State the blood parasite species.
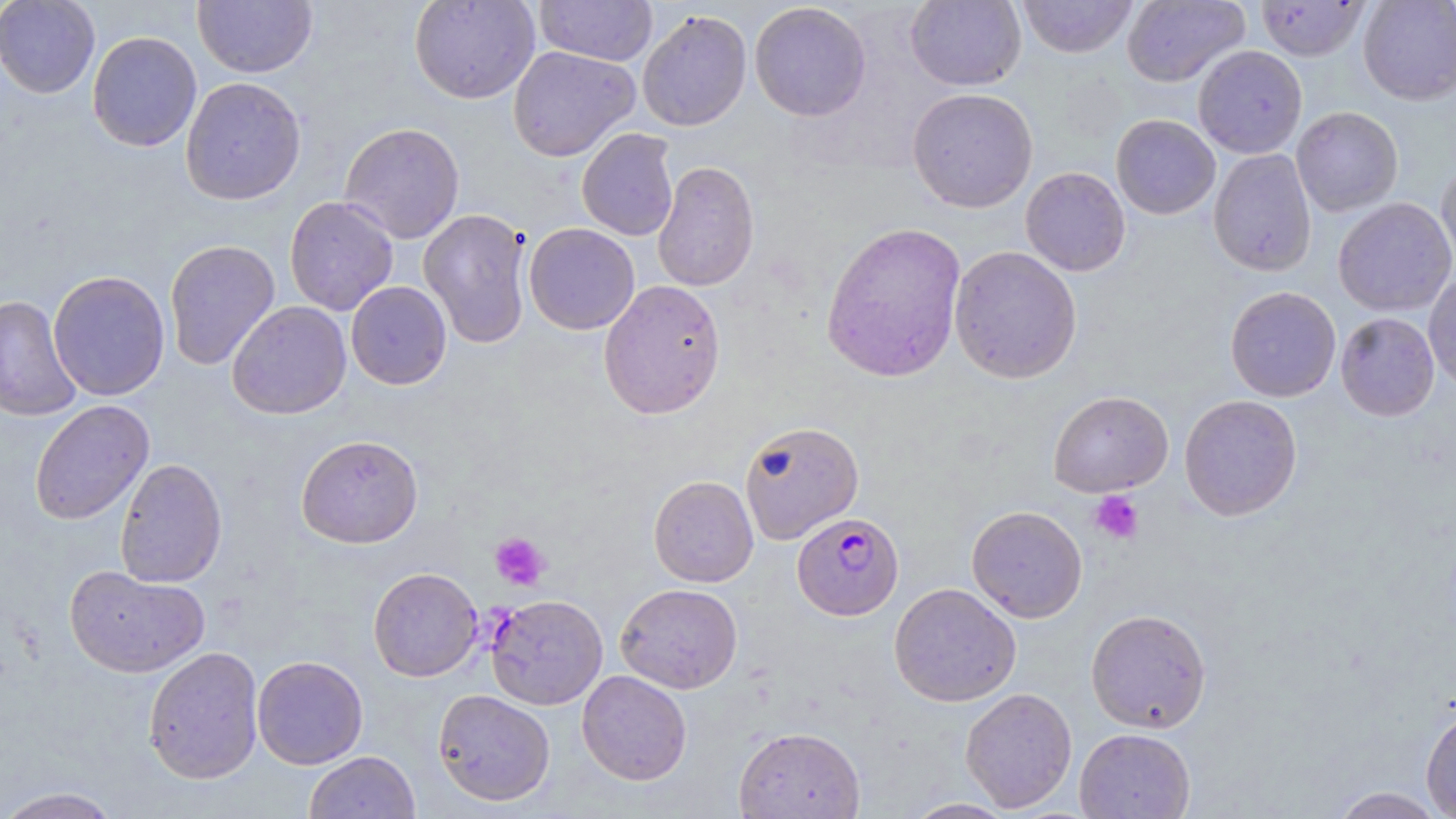
Plasmodium falciparum.

Summary:
  - Coordinate format: approximate bounding boxes as [x1, y1, x2, y2] in pixels
  - Plasmodium falciparum-infected red blood cell locations: [792, 512, 903, 620]
  - Uninfected red blood cell locations: [0, 0, 100, 98], [193, 0, 317, 78], [409, 0, 540, 104], [535, 0, 658, 66], [905, 0, 1026, 91], [1016, 0, 1139, 58], [1121, 0, 1249, 87], [1358, 0, 1456, 105], [1256, 1, 1370, 61], [749, 2, 872, 121], [637, 9, 752, 132], [87, 31, 202, 151], [1193, 45, 1307, 159], [507, 46, 639, 161], [180, 76, 307, 205], [907, 87, 1038, 213], [1291, 106, 1403, 216], [1110, 114, 1220, 219], [339, 122, 465, 244], [576, 128, 679, 241], [1208, 148, 1317, 277], [652, 160, 760, 292], [1436, 160, 1456, 273], [1020, 166, 1131, 276], [284, 196, 399, 316], [1333, 198, 1456, 316], [418, 208, 532, 348], [820, 221, 967, 383], [523, 222, 640, 335], [164, 239, 281, 370], [949, 245, 1082, 384], [48, 269, 170, 401], [1423, 271, 1456, 392], [598, 279, 726, 419], [346, 281, 452, 389], [1225, 286, 1341, 402], [0, 295, 83, 421], [227, 300, 351, 420], [1335, 312, 1440, 421], [1048, 391, 1174, 496], [1179, 394, 1302, 521], [30, 400, 154, 525], [738, 420, 864, 544], [296, 434, 423, 548], [114, 458, 227, 588], [648, 475, 758, 587], [966, 505, 1088, 622], [65, 565, 209, 677], [368, 567, 483, 682], [889, 582, 1021, 707], [616, 583, 743, 693], [486, 594, 608, 709], [1086, 609, 1212, 733], [143, 646, 264, 784], [252, 655, 368, 769], [577, 669, 692, 785], [960, 687, 1077, 812], [433, 689, 556, 806], [1421, 705, 1456, 816], [733, 726, 865, 818], [1074, 728, 1196, 818], [303, 751, 420, 819], [0, 786, 123, 819], [1327, 786, 1449, 818], [901, 797, 1016, 818]
  - Platelet locations: [1089, 490, 1144, 544], [490, 532, 549, 591]
  - Magnification: 1000x
  - Image size: 1456×819 pixels
  - Field of view: single
  - Modality: light microscopy
  - Stain: May-Grünwald-Giemsa
  - Preparation: thin blood smear